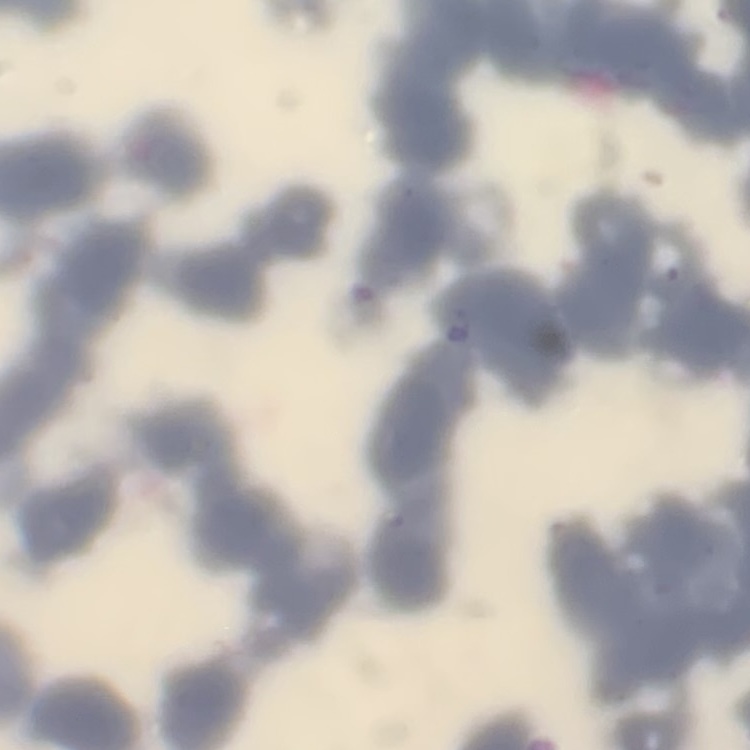
Summary:
  - Red blood cell morphology: rouleaux formation
  - Stain: Field's or Giemsa
  - Preparation: thin blood smear
  - Image type: square crop of a larger photomicrograph